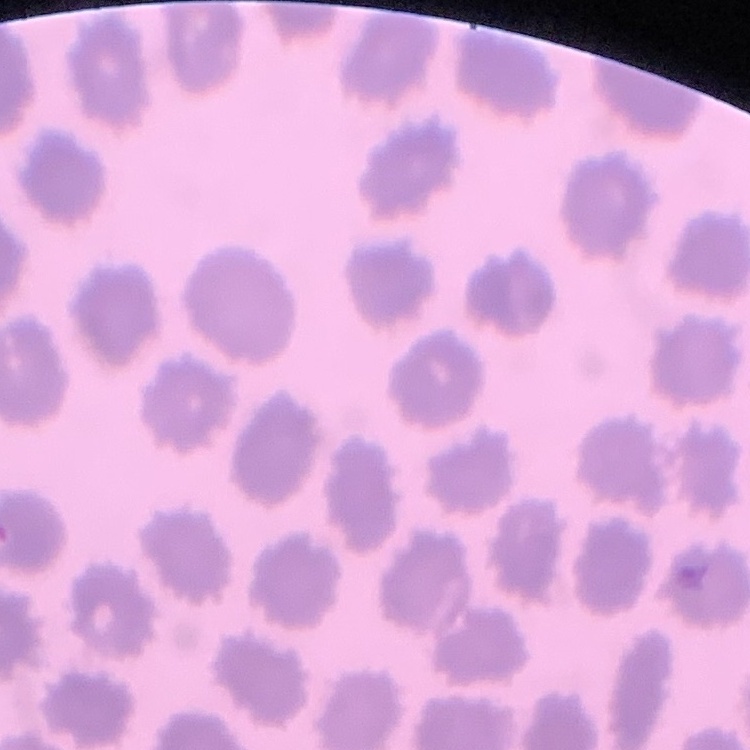

erythrocyte morphology = no rouleaux formation
stain = Field's or Giemsa
image type = square crop of a larger photomicrograph
preparation = thin blood film